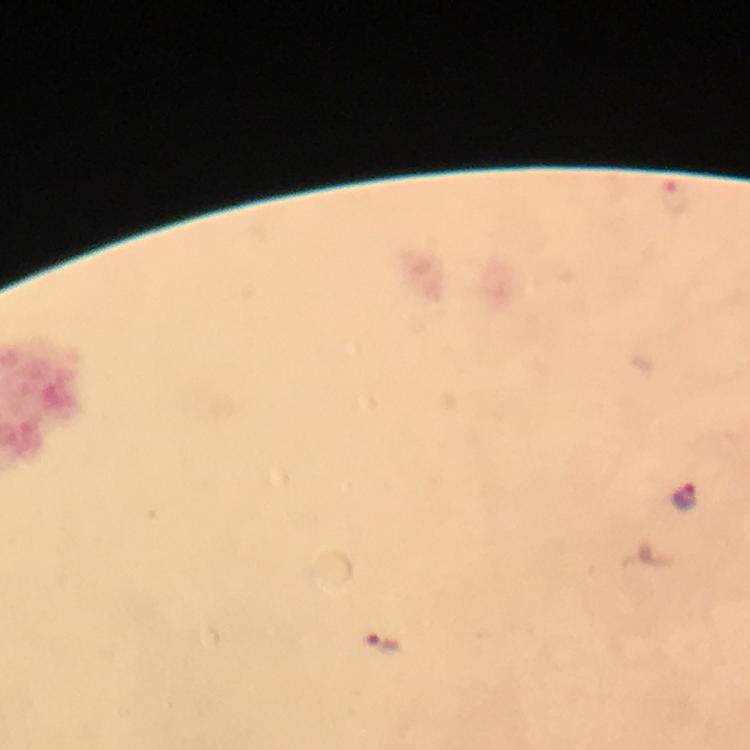

magnification = 100x
image size = 750×750 pixels
capture = smartphone photograph through a microscope
context = from a diagnostic examination for malaria
preparation = thick blood smear
cropped from = one field of view
stain = Giemsa
Plasmodium parasite locations = approximate centers as (x, y) in pixels: (676, 197), (682, 499), (382, 646)
immersion oil = used